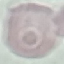
malaria status = uninfected
stain = Giemsa
capture = smartphone camera at the microscope eyepiece
preparation = thin smear
image type = cell patch, automatically extracted from a larger field of view and resized to 64 × 64 pixels